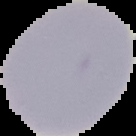 From a thin blood film. Result: negative for Plasmodium parasites. Segmented cell region on a black background. Image is 136×136 pixels.